Identify the parasite.
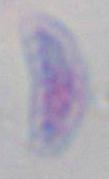

Toxoplasma gondii.

Micrograph. Captured at 1000x magnification.